Assess this cell for malaria.
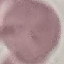
It is uninfected.

Automatically extracted cell patch, resized to 64 × 64 pixels. Thin blood smear. Photographed with a smartphone camera at the microscope eyepiece. Giemsa-stained preparation.